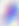
identification = Toxoplasma gondii
magnification = 400x
modality = micrograph